State which parasite is depicted.
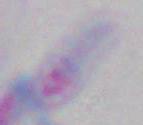
This is Toxoplasma gondii.

Summary:
  - Modality: photomicrograph
  - Magnification: 1000x